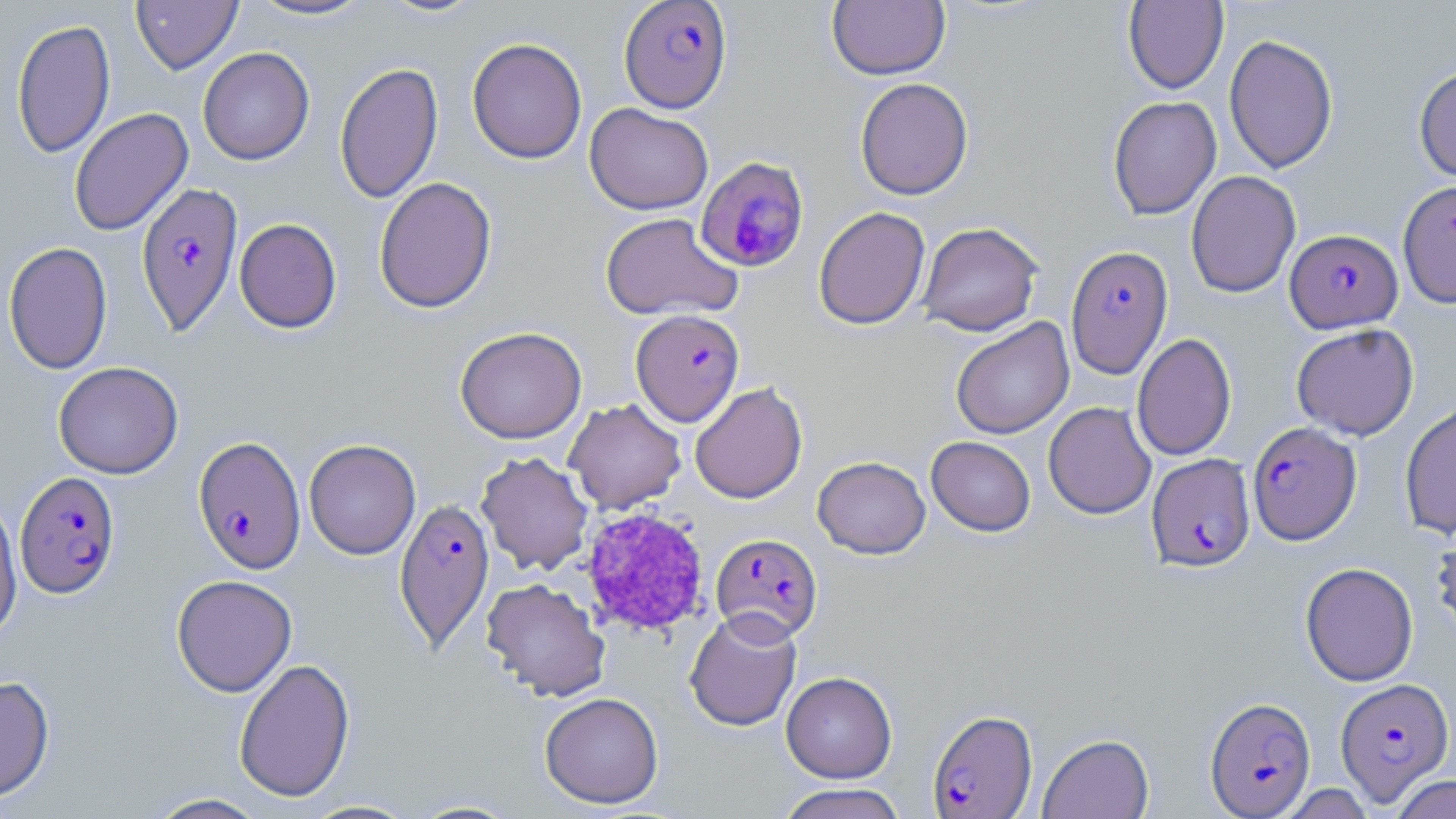
Summary:
  - Coordinate format: approximate bounding boxes as (x1, y1, x2, y2) in pixels
  - Platelet locations: (579, 507, 710, 637)
  - Uninfected red blood cell locations: (131, 0, 242, 75), (246, 0, 377, 21), (376, 0, 488, 19), (827, 1, 950, 80), (1123, 1, 1228, 94), (11, 18, 115, 158), (1223, 34, 1339, 174), (466, 37, 587, 164), (197, 46, 314, 165), (334, 61, 443, 204), (1413, 63, 1456, 183), (855, 77, 973, 200), (1107, 95, 1221, 220), (585, 103, 713, 215), (68, 108, 193, 236), (1186, 170, 1301, 297), (374, 176, 497, 313), (1398, 179, 1456, 307), (813, 206, 930, 330), (600, 212, 742, 321), (234, 218, 342, 333), (917, 222, 1043, 336), (3, 241, 113, 374), (951, 317, 1074, 440), (1291, 323, 1419, 440), (454, 326, 586, 443), (1132, 332, 1236, 461), (53, 361, 183, 479), (690, 381, 808, 504), (563, 398, 686, 515), (1043, 401, 1156, 519), (1400, 401, 1456, 539), (926, 436, 1036, 537), (304, 438, 421, 559), (476, 451, 594, 576), (813, 456, 930, 558), (0, 494, 22, 645), (1430, 520, 1456, 642), (1300, 562, 1418, 686), (171, 574, 297, 697), (481, 578, 611, 702), (684, 609, 802, 731), (233, 657, 356, 803), (781, 671, 897, 783), (0, 674, 55, 802), (539, 692, 664, 809), (1038, 733, 1154, 819), (1388, 774, 1456, 819), (774, 783, 910, 819), (1275, 784, 1377, 818), (144, 793, 270, 818), (406, 798, 524, 818), (299, 799, 422, 818)
  - Plasmodium falciparum-infected red blood cell locations: (619, 1, 732, 113), (695, 157, 809, 273), (135, 180, 244, 338), (1285, 228, 1402, 332), (1065, 245, 1173, 379), (631, 309, 744, 426), (1248, 421, 1361, 545), (192, 436, 306, 574), (1147, 452, 1255, 573), (15, 470, 121, 598), (393, 497, 495, 654), (710, 533, 823, 642), (1335, 677, 1455, 804), (1204, 696, 1316, 817), (927, 708, 1038, 817)
  - Slide-level diagnosis: Plasmodium falciparum
  - Preparation: thin blood film
  - Stain: May-Grünwald-Giemsa
  - Image size: 1456×819 pixels
  - Field of view: one of a larger specimen
  - Modality: optical microscopy
  - Magnification: 1000x